Outline each blood parasite and name the species.
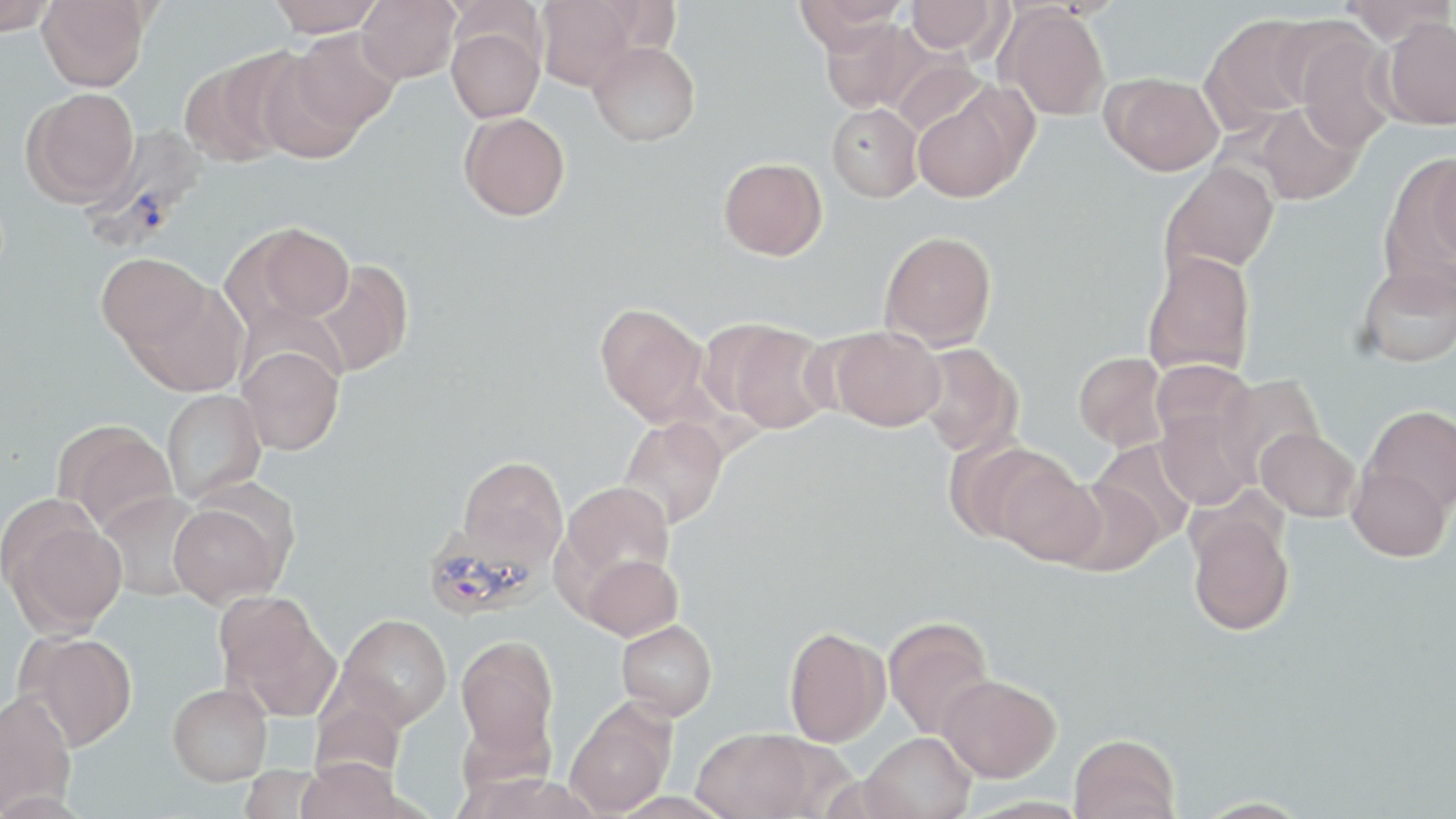
Approximate bounding boxes as (x1, y1, x2, y2) in pixels.
Plasmodium vivax-infected red blood cells: (82, 125, 206, 257), (423, 517, 546, 621).
No Plasmodium falciparum, Plasmodium ovale, Plasmodium malariae, Babesia divergens, or Trypanosoma brucei observed.

Summary:
  - Uninfected red blood cell locations: (0, 0, 57, 35), (36, 0, 153, 91), (267, 0, 384, 37), (357, 0, 461, 84), (535, 0, 644, 91), (905, 0, 1004, 54), (1339, 0, 1455, 44), (793, 1, 907, 50), (997, 5, 1111, 121), (1200, 14, 1322, 132), (1381, 16, 1456, 129), (819, 17, 928, 114), (446, 25, 545, 123), (290, 28, 401, 133), (1294, 30, 1398, 153), (588, 40, 700, 146), (253, 49, 368, 164), (179, 55, 296, 167), (1103, 73, 1224, 176), (911, 86, 1034, 203), (21, 88, 139, 207), (1249, 102, 1363, 205), (826, 103, 923, 202), (459, 112, 570, 221), (1384, 152, 1455, 281), (1428, 153, 1456, 269), (719, 157, 827, 260), (1160, 162, 1279, 278), (228, 221, 355, 329), (880, 230, 997, 351), (1142, 250, 1256, 378), (97, 252, 210, 353), (310, 259, 413, 377), (1356, 260, 1456, 368), (126, 280, 249, 397), (594, 302, 711, 425), (711, 320, 834, 433), (828, 326, 946, 431), (915, 343, 1022, 457), (238, 345, 345, 455), (1074, 352, 1168, 451), (1150, 359, 1255, 450), (1214, 375, 1323, 483), (162, 389, 267, 503), (1364, 405, 1456, 512), (1156, 408, 1259, 509), (618, 417, 729, 530), (58, 421, 178, 533), (1257, 427, 1361, 521), (1090, 438, 1197, 546), (943, 439, 1054, 543), (457, 455, 568, 566), (991, 455, 1105, 566), (1348, 463, 1450, 561), (1057, 478, 1164, 576), (556, 480, 677, 602), (96, 491, 208, 602), (167, 499, 290, 608), (4, 508, 128, 634), (1186, 510, 1294, 636), (582, 554, 682, 640), (216, 593, 339, 718), (337, 614, 452, 728), (883, 616, 994, 739), (616, 620, 717, 720), (784, 626, 891, 747), (21, 632, 137, 750), (455, 635, 558, 758), (938, 675, 1060, 782), (168, 682, 272, 785), (1, 690, 76, 815), (565, 699, 677, 817), (692, 727, 822, 818), (861, 732, 976, 819), (1069, 733, 1180, 819), (295, 757, 408, 819)
  - Slide-level diagnosis: Plasmodium vivax
  - Stain: May-Grünwald-Giemsa
  - Magnification: 1000x
  - Preparation: thin blood smear
  - Modality: light microscopy
  - Image size: 1456×819 pixels
  - Field of view: single